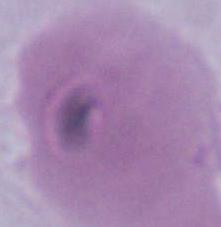

Summary:
  - Identification: red blood cell
  - Modality: micrograph
  - Magnification: 1000x